Classify this cell by malaria status.
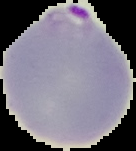
It is parasitized.

image size = 136×151 pixels
preparation = thin blood film
image type = segmented cell region on a black background